Describe the morphology of the erythrocytes.
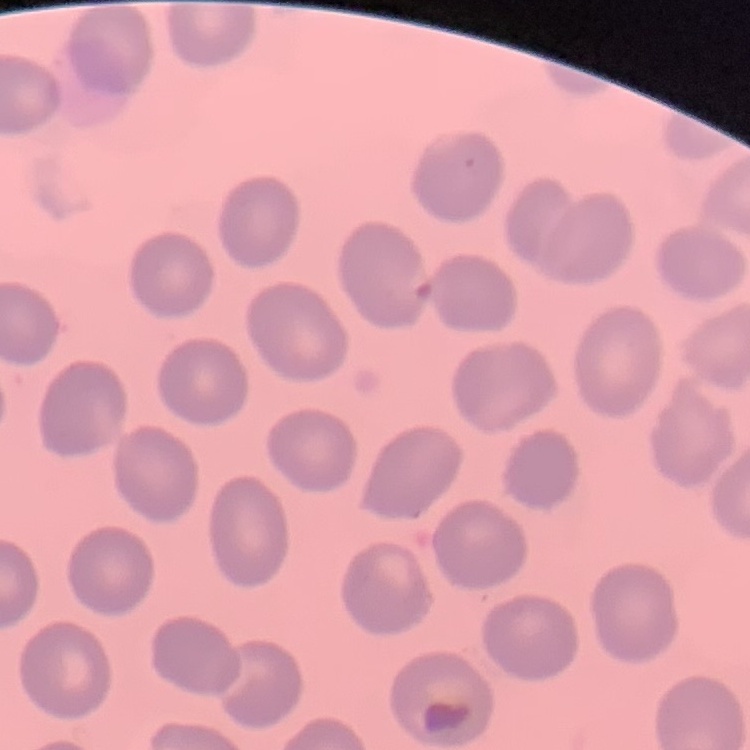
They show no rouleaux formation.

Summary:
  - Preparation: thin blood film
  - Image type: one tile cut from a larger photomicrograph
  - Stain: Field's or Giemsa